State which cell type is depicted.
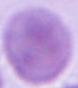
An erythrocyte.

magnification = 1000x
modality = photomicrograph